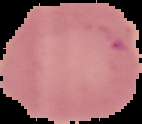

Summary:
  - Preparation: thin blood smear
  - Result: negative for malaria parasites
  - Image size: 142×124 pixels
  - Image type: cell region segmented out of the field of view; surrounding area masked to black